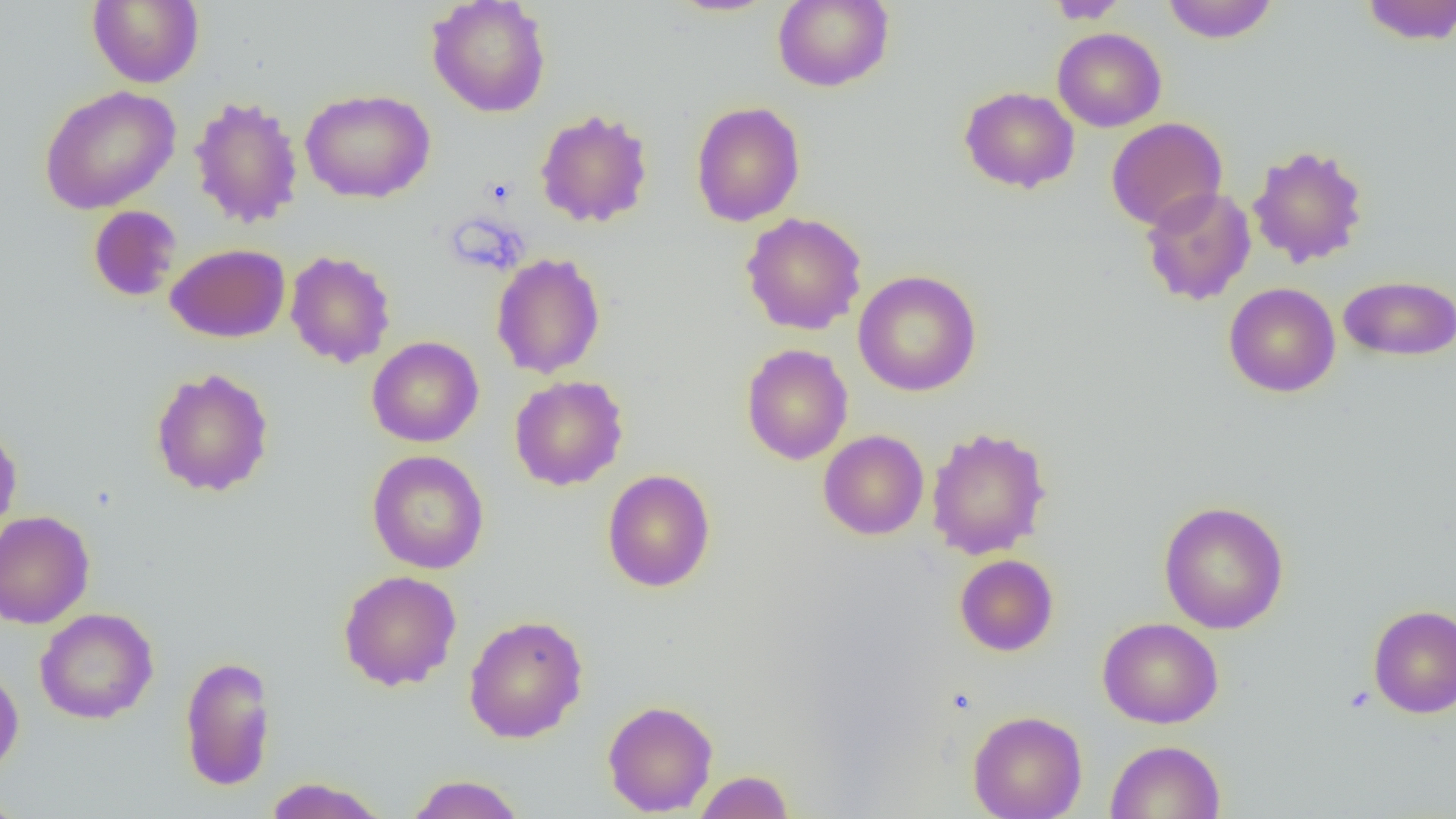

Summary:
  - Coordinate format: approximate bounding boxes as (x1,y1)-(x2,y2) corner pairs in pixels
  - Platelet locations: (483,176)-(516,208)
  - Uninfected red blood cell locations: (87,0)-(204,88), (665,0)-(779,17), (772,0)-(894,92), (1047,0)-(1129,24), (1161,0)-(1278,43), (1358,0)-(1456,46), (426,1)-(551,117), (1052,27)-(1166,132), (38,85)-(181,214), (959,86)-(1079,193), (300,88)-(436,204), (188,95)-(304,229), (691,101)-(805,227), (535,109)-(653,228), (1106,117)-(1228,231), (1247,143)-(1369,268), (1141,187)-(1256,306), (88,205)-(182,302), (740,212)-(868,335), (166,243)-(290,343), (285,250)-(396,368), (491,252)-(606,379), (853,270)-(982,396), (1338,275)-(1456,362), (1224,282)-(1340,397), (367,336)-(483,447), (741,343)-(853,465), (150,367)-(274,497), (509,375)-(628,491), (0,422)-(22,542), (926,426)-(1052,560), (818,430)-(929,540), (367,450)-(489,574), (602,469)-(716,592), (1158,500)-(1289,634), (0,511)-(95,629), (954,554)-(1058,656), (338,569)-(462,691), (1368,604)-(1456,718), (34,607)-(159,724), (463,614)-(588,744), (1097,617)-(1224,729), (179,654)-(277,792), (0,665)-(24,779), (603,699)-(718,816), (967,710)-(1087,819), (1105,739)-(1226,818), (693,770)-(794,818), (405,774)-(525,819), (263,777)-(390,819), (0,789)-(27,819)
  - Slide-level diagnosis: negative for blood parasites
  - Preparation: thin blood smear
  - Image size: 1456×819 pixels
  - Field of view: one of a larger specimen
  - Modality: optical microscopy
  - Magnification: 1000x